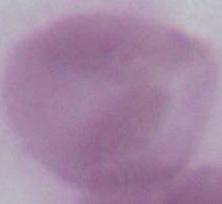

Summary:
  - Magnification: 1000x
  - Identification: red blood cell
  - Modality: micrograph